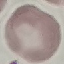
result: no malaria parasites detected
capture: smartphone camera at the microscope eyepiece
preparation: thin blood film
image_type: automatically extracted cell patch, resized to 64 × 64 pixels
stain: Giemsa